State which cell type is depicted.
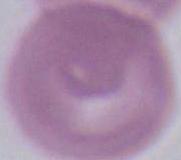

This is an erythrocyte.

Captured at 1000x magnification. Micrograph.